Report the malaria status of this cell.
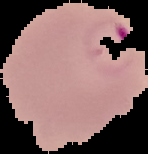
It is parasitized.

{
  "image_type": "segmented cell region with the area outside set to black",
  "preparation": "thin blood film",
  "image_size": "148×154 pixels"
}